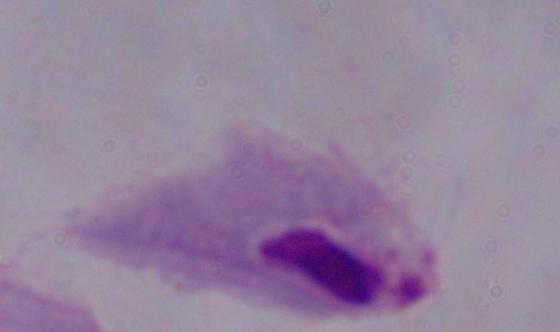
A trichomonad is shown. Micrograph. Captured at 1000x magnification.